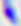 Captured at 400x magnification. Toxoplasma gondii is shown. Photomicrograph.